Classify this cell by malaria status.
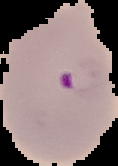
It is parasitized.

From a thin blood film. Image is 118×166 pixels. Segmented cell region on a black background.